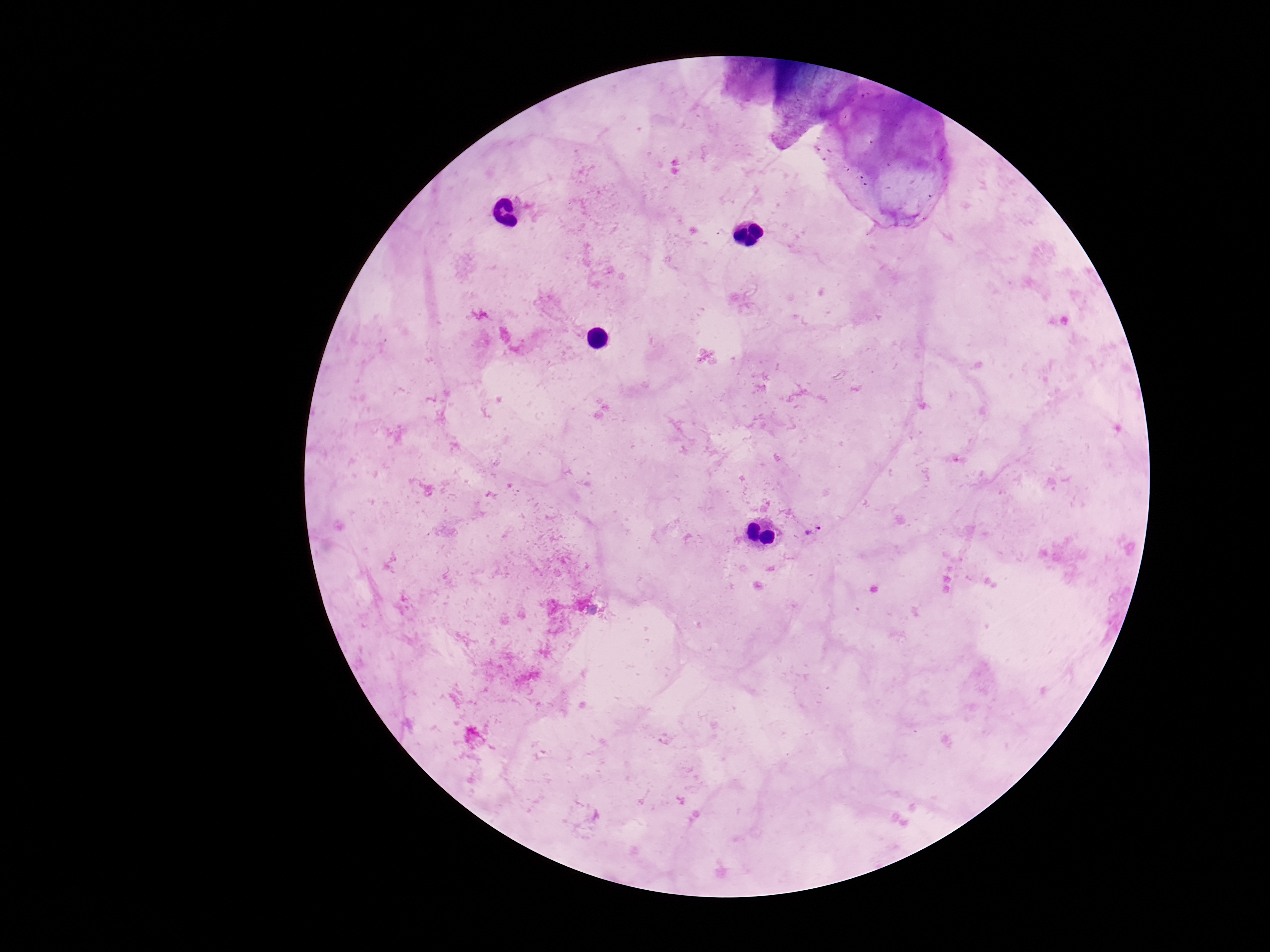

patient malaria status = infected
image size = 1270×952 pixels
magnification = 100x
capture = smartphone camera through the microscope eyepiece
field of view = one from this slide
preparation = thick blood smear
Plasmodium parasite locations = approximate centers as (x, y) in pixels: (812, 530)
stain = Giemsa